Classify this cell by malaria status.
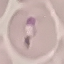

Parasitized.

Summary:
  - Image type: cell patch, automatically extracted from a larger field of view and resized to 64 × 64 pixels
  - Capture: smartphone through the microscope eyepiece
  - Preparation: thin blood film
  - Stain: Giemsa